Locate and identify every blood parasite.
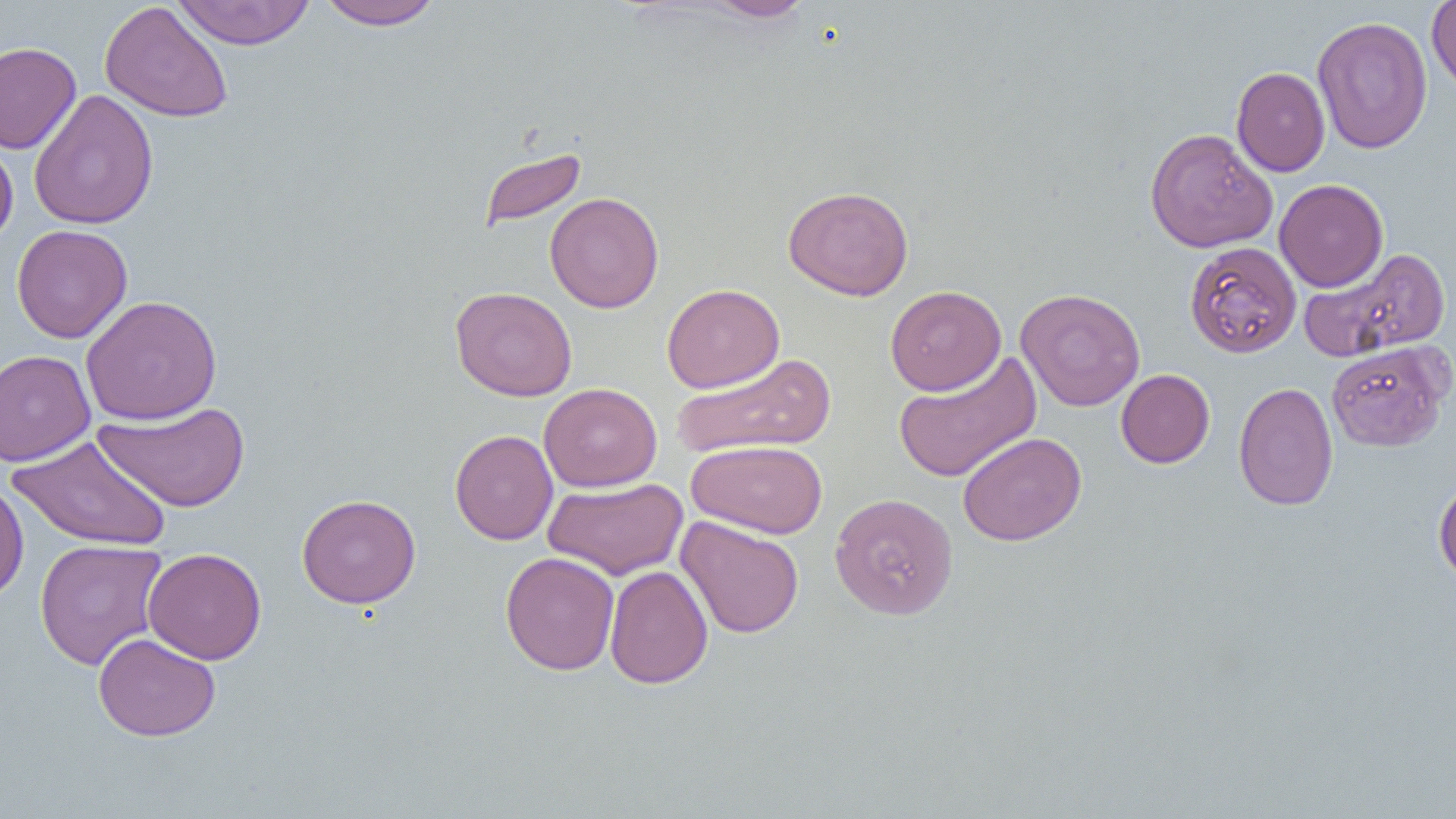

No blood parasites seen.

slide-level diagnosis = negative for blood parasites
image size = 1456×819 pixels
uninfected red blood cell locations = approximate bounding boxes as [x1, y1, x2, y2] in pixels: [171, 0, 316, 49], [315, 0, 445, 31], [700, 0, 814, 23], [1427, 0, 1456, 97], [99, 1, 234, 123], [1312, 16, 1433, 154], [0, 42, 81, 155], [1231, 66, 1330, 177], [29, 88, 159, 229], [1144, 127, 1278, 253], [0, 137, 18, 248], [477, 146, 587, 231], [1274, 178, 1389, 292], [783, 185, 914, 300], [544, 192, 664, 313], [11, 224, 132, 343], [1185, 241, 1301, 359], [1301, 247, 1451, 360], [661, 283, 785, 393], [885, 285, 1006, 395], [450, 286, 577, 401], [1015, 288, 1146, 412], [81, 295, 221, 425], [1326, 340, 1452, 452], [0, 349, 95, 466], [893, 350, 1042, 484], [670, 353, 836, 460], [1116, 369, 1215, 468], [1233, 381, 1338, 510], [539, 383, 662, 492], [94, 401, 251, 513], [450, 429, 558, 545], [958, 431, 1086, 546], [7, 435, 172, 551], [686, 440, 828, 538], [1433, 476, 1456, 586], [542, 477, 688, 581], [0, 479, 29, 602], [829, 492, 959, 620], [297, 494, 421, 609], [676, 516, 804, 639], [34, 538, 169, 670], [143, 547, 266, 665], [500, 551, 619, 675], [605, 565, 713, 689], [93, 632, 221, 741]
magnification = 1000x
modality = optical microscopy
field of view = one of a larger specimen
preparation = thin blood smear